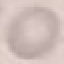 Result: negative for malaria parasites. Automatically extracted cell patch, resized to 64 × 64 pixels. Thin blood film. Giemsa-stained preparation. Photographed with a smartphone camera at the microscope eyepiece.